Outline each uninfected red blood cell.
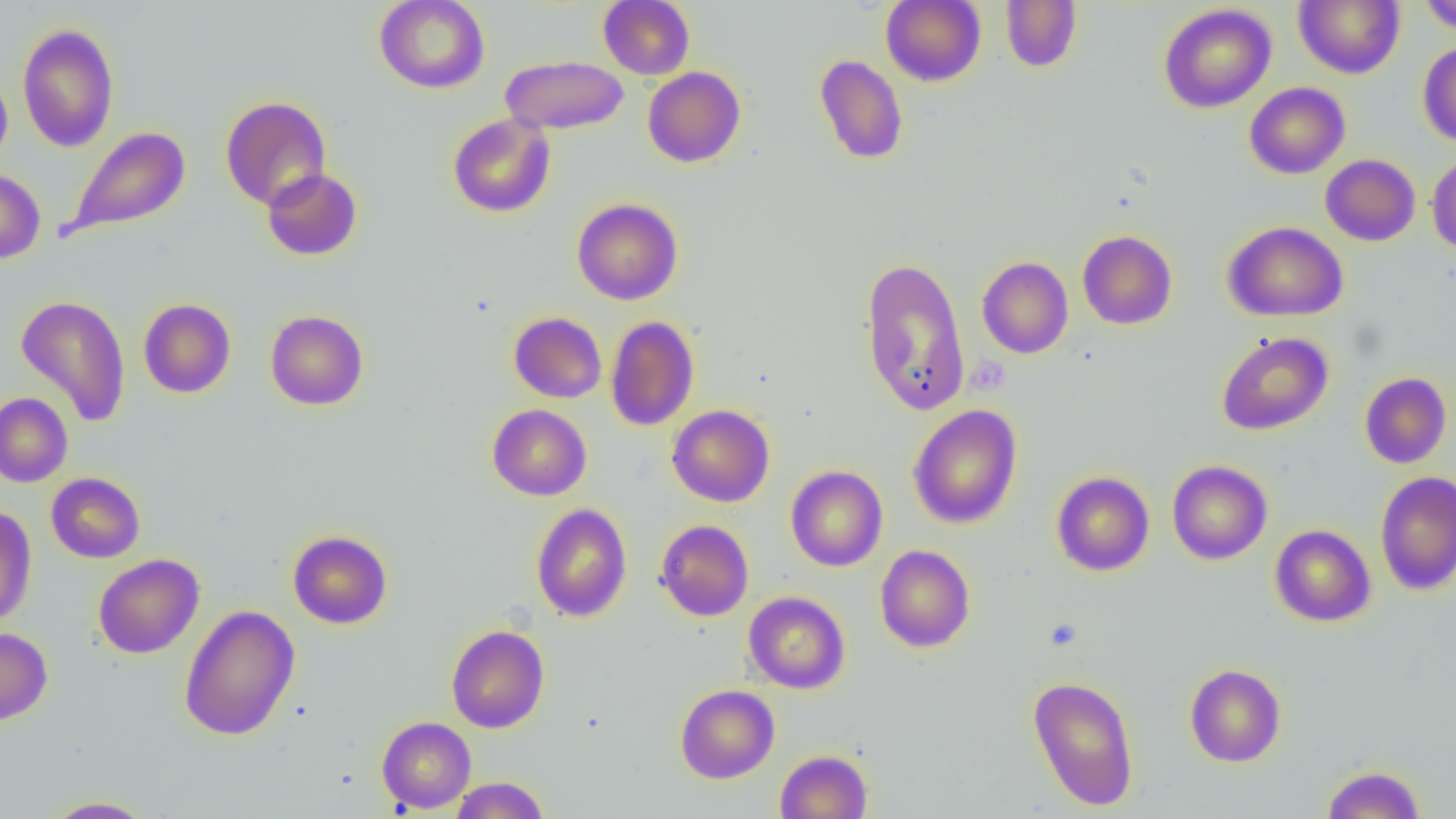
Approximate bounding boxes as named x1/y1/x2/y2 corners in pixels.
Uninfected red blood cells: (x1=374, y1=0, x2=490, y2=93), (x1=598, y1=0, x2=695, y2=79), (x1=881, y1=0, x2=985, y2=86), (x1=1001, y1=0, x2=1082, y2=73), (x1=1294, y1=0, x2=1405, y2=79), (x1=1419, y1=0, x2=1456, y2=35), (x1=1158, y1=4, x2=1276, y2=113), (x1=17, y1=22, x2=119, y2=153), (x1=1418, y1=42, x2=1456, y2=147), (x1=814, y1=54, x2=908, y2=165), (x1=500, y1=55, x2=629, y2=135), (x1=0, y1=65, x2=13, y2=171), (x1=642, y1=67, x2=745, y2=167), (x1=1244, y1=82, x2=1350, y2=179), (x1=220, y1=95, x2=331, y2=210), (x1=447, y1=113, x2=556, y2=218), (x1=63, y1=126, x2=191, y2=239), (x1=1321, y1=154, x2=1420, y2=246), (x1=1427, y1=154, x2=1456, y2=254), (x1=0, y1=167, x2=45, y2=264), (x1=261, y1=167, x2=362, y2=260), (x1=571, y1=198, x2=683, y2=305), (x1=1223, y1=221, x2=1349, y2=321), (x1=1077, y1=230, x2=1177, y2=330), (x1=860, y1=256, x2=971, y2=417), (x1=977, y1=256, x2=1073, y2=359), (x1=15, y1=294, x2=131, y2=427), (x1=138, y1=298, x2=236, y2=398), (x1=265, y1=309, x2=368, y2=411), (x1=508, y1=311, x2=607, y2=403), (x1=605, y1=316, x2=700, y2=431), (x1=1216, y1=331, x2=1333, y2=436), (x1=1360, y1=372, x2=1451, y2=468), (x1=0, y1=392, x2=72, y2=487), (x1=487, y1=404, x2=592, y2=500), (x1=908, y1=404, x2=1023, y2=529), (x1=668, y1=405, x2=775, y2=507), (x1=1167, y1=460, x2=1272, y2=565), (x1=785, y1=465, x2=888, y2=571), (x1=1051, y1=471, x2=1154, y2=576), (x1=46, y1=472, x2=145, y2=563), (x1=1375, y1=472, x2=1455, y2=595), (x1=531, y1=503, x2=632, y2=622), (x1=0, y1=506, x2=36, y2=627), (x1=655, y1=519, x2=754, y2=621), (x1=1270, y1=524, x2=1376, y2=627), (x1=287, y1=529, x2=393, y2=629), (x1=875, y1=544, x2=975, y2=652), (x1=93, y1=554, x2=204, y2=659), (x1=744, y1=591, x2=850, y2=693), (x1=179, y1=604, x2=300, y2=741), (x1=446, y1=624, x2=549, y2=733), (x1=0, y1=627, x2=52, y2=725), (x1=1185, y1=664, x2=1286, y2=767), (x1=1027, y1=675, x2=1140, y2=810), (x1=675, y1=684, x2=779, y2=783), (x1=377, y1=716, x2=476, y2=813), (x1=775, y1=750, x2=873, y2=819), (x1=1321, y1=764, x2=1426, y2=819), (x1=449, y1=776, x2=549, y2=819), (x1=42, y1=796, x2=155, y2=818).

Slide-level diagnosis: negative for blood parasites. Image is 1456×819 pixels. Light microscopy. One field of a larger specimen. Thin blood film. Captured at 1000x magnification.